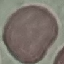
Summary:
  - Malaria status: uninfected
  - Capture: smartphone camera at the microscope eyepiece
  - Image type: automatically extracted cell patch, resized to 64 × 64 pixels
  - Stain: Giemsa
  - Preparation: thin smear